Describe the morphology of the red blood cells.
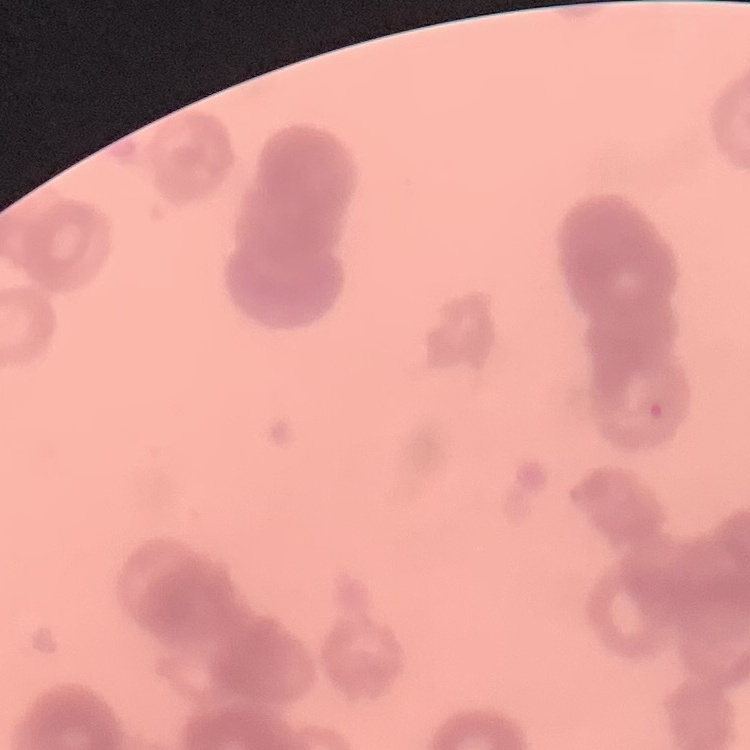
Rouleaux formation.

Square crop of a larger photomicrograph. Thin blood film. Stained with either Field's or Giemsa.